Describe the morphology of the erythrocytes.
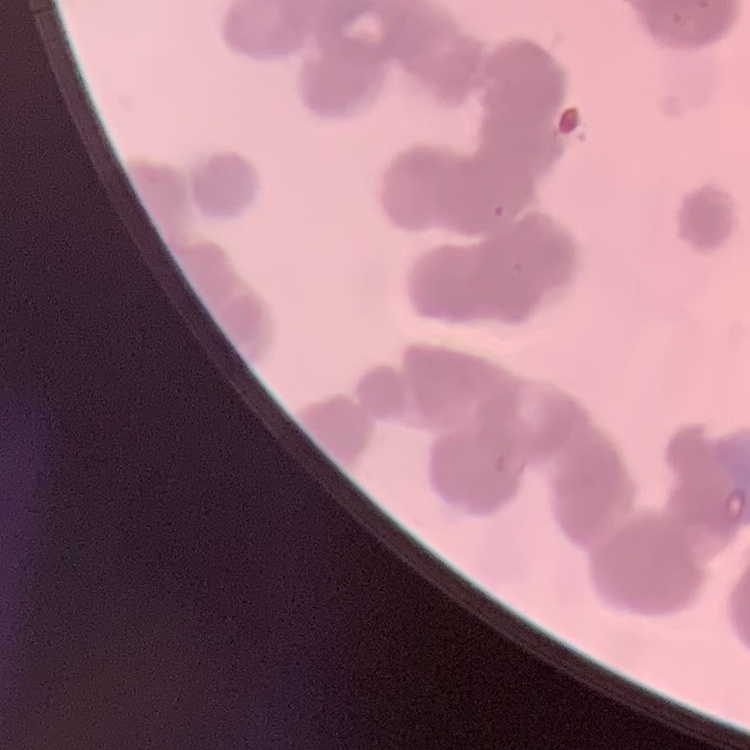
They show rouleaux formation.

Summary:
  - Preparation: thin blood smear
  - Image type: one tile cut from a larger photomicrograph
  - Stain: Field's or Giemsa